State which parasite is depicted.
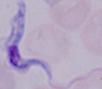
This is a trypanosome.

Micrograph. Captured at 1000x magnification.